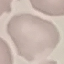
Malaria status: uninfected. Thin blood film. Photographed with a smartphone camera at the microscope eyepiece. Cell patch, automatically extracted from a larger field of view and resized to 64 × 64 pixels. Giemsa-stained preparation.